Classify this cell by malaria status.
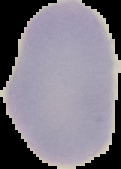
Uninfected.

image size = 121×169 pixels
preparation = thin blood film
image type = cell region segmented out of the field of view; surrounding area masked to black